Identify the parasite.
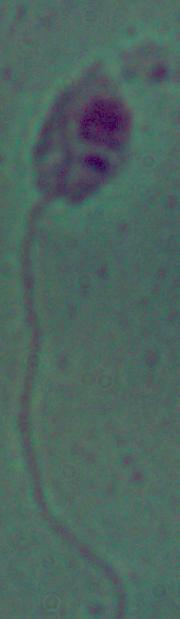

This is Leishmania.

magnification = 1000x
modality = photomicrograph